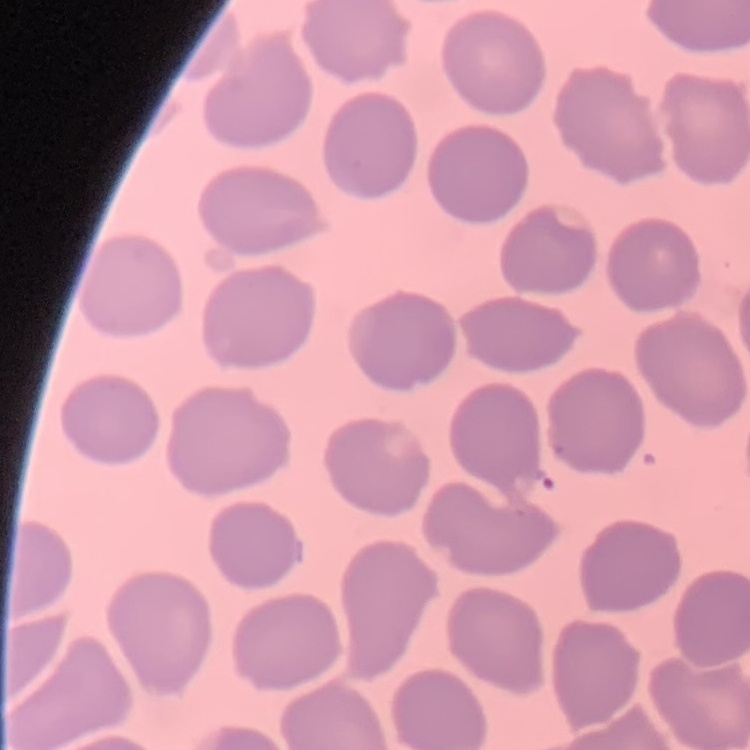
red_blood_cell_morphology: no rouleaux formation
preparation: thin blood smear
image_type: one tile cut from a larger photomicrograph
stain: Field's or Giemsa